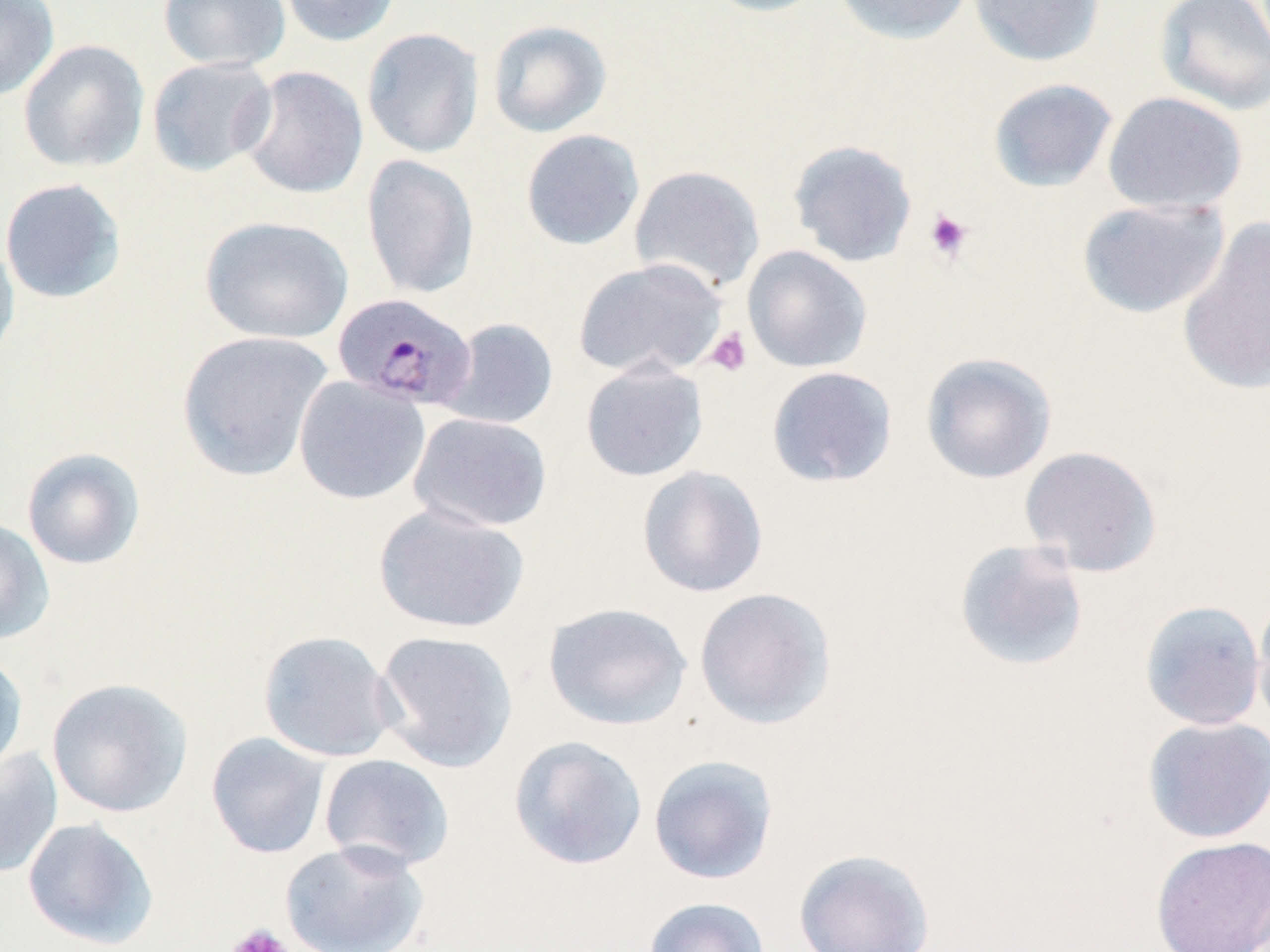
slide_level_diagnosis: Plasmodium malariae
image_size: 1270×952 pixels
modality: light microscopy
plasmodium_malariae_infected_red_blood_cell_locations: 'approximate bounding boxes as (x1, y1, x2, y2) in pixels: (335, 295, 481, 415)'
field_of_view: one of a larger specimen
uninfected_red_blood_cell_locations: 'approximate bounding boxes as (x1, y1, x2, y2) in pixels: (0, 0, 59, 101), (157, 0, 292, 72), (276, 0, 402, 47), (699, 0, 831, 18), (833, 0, 975, 45), (968, 0, 1105, 67), (1154, 0, 1270, 116), (487, 19, 612, 138), (362, 27, 484, 159), (17, 40, 150, 173), (146, 56, 278, 177), (238, 65, 369, 199), (987, 78, 1118, 192), (1103, 91, 1248, 214), (520, 129, 645, 251), (787, 139, 917, 268), (360, 154, 479, 299), (629, 164, 765, 295), (0, 178, 127, 304), (1076, 198, 1229, 318), (199, 215, 353, 344), (1176, 218, 1270, 396), (0, 232, 20, 367), (742, 245, 872, 373), (572, 257, 728, 381), (440, 318, 559, 430), (175, 330, 334, 482), (920, 352, 1057, 484), (580, 360, 708, 482), (766, 366, 898, 488), (293, 375, 430, 505), (409, 412, 553, 532), (1018, 445, 1163, 577), (21, 447, 145, 570), (637, 465, 769, 598), (373, 503, 530, 634), (0, 518, 55, 645), (953, 538, 1090, 672), (693, 587, 837, 730), (1252, 588, 1270, 732), (1139, 599, 1266, 731), (542, 602, 693, 731), (257, 630, 398, 763), (373, 630, 518, 773), (0, 651, 29, 778), (46, 678, 193, 818), (1142, 716, 1270, 844), (206, 732, 330, 859), (508, 735, 648, 871), (0, 746, 63, 880), (318, 753, 454, 872), (648, 754, 779, 885), (22, 817, 159, 950), (1149, 836, 1270, 951), (279, 839, 430, 952), (793, 848, 936, 951), (642, 896, 771, 952)'
platelet_locations: 'approximate bounding boxes as (x1, y1, x2, y2) in pixels: (923, 208, 974, 262), (705, 326, 753, 377), (225, 924, 294, 952)'
preparation: thin blood film
stain: May-Grünwald-Giemsa
magnification: 1000x